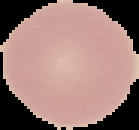
image size = 139×130 pixels
image type = cell region segmented out of the field of view; surrounding area masked to black
preparation = thin blood smear
malaria status = uninfected